Classify this cell by malaria status.
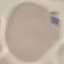
It is uninfected.

Giemsa stain. Photographed with a smartphone camera at the microscope eyepiece. Thin blood film. Automatically extracted cell patch, resized to 64 × 64 pixels.